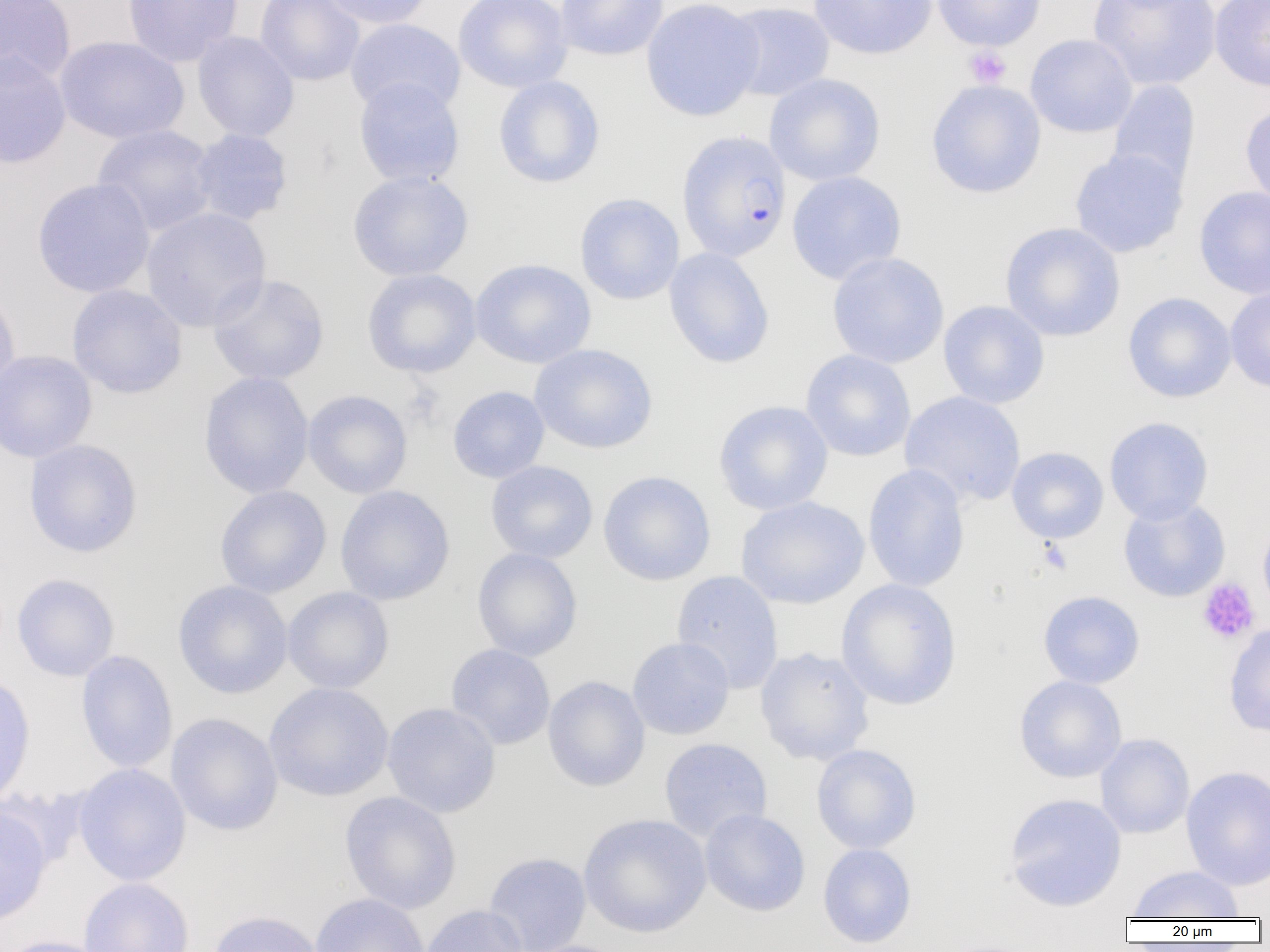

Summary:
  - Coordinate format: approximate bounding boxes as named x1/y1/x2/y2 corners in pixels
  - Uninfected red blood cell locations (subset): (x1=0, y1=0, x2=76, y2=87), (x1=122, y1=0, x2=243, y2=67), (x1=256, y1=0, x2=365, y2=86), (x1=319, y1=0, x2=431, y2=28), (x1=453, y1=0, x2=572, y2=93), (x1=555, y1=0, x2=669, y2=61), (x1=641, y1=0, x2=765, y2=121), (x1=808, y1=0, x2=938, y2=60), (x1=932, y1=0, x2=1046, y2=51), (x1=1210, y1=0, x2=1270, y2=92), (x1=1088, y1=1, x2=1221, y2=90), (x1=722, y1=2, x2=835, y2=101), (x1=345, y1=18, x2=465, y2=117), (x1=192, y1=31, x2=299, y2=142), (x1=1025, y1=34, x2=1138, y2=138), (x1=54, y1=36, x2=189, y2=144), (x1=0, y1=51, x2=72, y2=169), (x1=764, y1=73, x2=885, y2=186), (x1=493, y1=75, x2=606, y2=188), (x1=353, y1=77, x2=465, y2=188), (x1=926, y1=79, x2=1046, y2=199), (x1=1107, y1=79, x2=1201, y2=192), (x1=1240, y1=100, x2=1270, y2=211), (x1=92, y1=124, x2=218, y2=237), (x1=187, y1=128, x2=294, y2=226), (x1=1069, y1=148, x2=1188, y2=258), (x1=347, y1=171, x2=473, y2=281), (x1=786, y1=171, x2=907, y2=284), (x1=32, y1=178, x2=155, y2=298), (x1=1194, y1=185, x2=1270, y2=300), (x1=574, y1=193, x2=685, y2=305), (x1=141, y1=207, x2=272, y2=332), (x1=1000, y1=222, x2=1125, y2=342), (x1=663, y1=247, x2=775, y2=368), (x1=827, y1=252, x2=949, y2=368), (x1=470, y1=258, x2=596, y2=368), (x1=361, y1=268, x2=482, y2=378), (x1=207, y1=273, x2=329, y2=385), (x1=66, y1=284, x2=188, y2=399), (x1=1225, y1=284, x2=1270, y2=394), (x1=0, y1=285, x2=21, y2=404), (x1=1123, y1=292, x2=1237, y2=403), (x1=938, y1=300, x2=1050, y2=409), (x1=529, y1=343, x2=658, y2=454), (x1=0, y1=349, x2=98, y2=463), (x1=801, y1=349, x2=916, y2=462), (x1=198, y1=371, x2=314, y2=499), (x1=447, y1=385, x2=550, y2=483), (x1=302, y1=389, x2=413, y2=499), (x1=899, y1=391, x2=1026, y2=508), (x1=713, y1=400, x2=833, y2=515), (x1=1104, y1=416, x2=1214, y2=524), (x1=23, y1=439, x2=143, y2=558), (x1=1006, y1=446, x2=1109, y2=544), (x1=485, y1=460, x2=598, y2=563), (x1=862, y1=464, x2=971, y2=592), (x1=481, y1=466, x2=714, y2=568), (x1=597, y1=470, x2=716, y2=586), (x1=214, y1=485, x2=332, y2=599), (x1=335, y1=485, x2=455, y2=605), (x1=735, y1=496, x2=870, y2=609), (x1=1257, y1=517, x2=1270, y2=623), (x1=472, y1=547, x2=583, y2=662), (x1=670, y1=570, x2=784, y2=693), (x1=12, y1=573, x2=120, y2=682), (x1=836, y1=578, x2=962, y2=710), (x1=172, y1=580, x2=293, y2=699), (x1=282, y1=587, x2=394, y2=694), (x1=1038, y1=590, x2=1145, y2=689), (x1=1224, y1=622, x2=1270, y2=737), (x1=627, y1=637, x2=735, y2=740), (x1=446, y1=644, x2=556, y2=750), (x1=754, y1=647, x2=875, y2=766), (x1=75, y1=650, x2=178, y2=773), (x1=0, y1=671, x2=35, y2=811), (x1=1014, y1=675, x2=1127, y2=783), (x1=542, y1=676, x2=650, y2=792), (x1=263, y1=682, x2=394, y2=802), (x1=382, y1=702, x2=501, y2=818), (x1=165, y1=713, x2=283, y2=836), (x1=1095, y1=733, x2=1194, y2=839), (x1=658, y1=737, x2=772, y2=842), (x1=811, y1=743, x2=922, y2=854), (x1=73, y1=763, x2=192, y2=886), (x1=1180, y1=765, x2=1270, y2=890), (x1=339, y1=791, x2=462, y2=915), (x1=1004, y1=793, x2=1127, y2=911), (x1=0, y1=804, x2=53, y2=928), (x1=700, y1=808, x2=811, y2=917), (x1=578, y1=813, x2=712, y2=938), (x1=817, y1=843, x2=917, y2=948), (x1=483, y1=852, x2=592, y2=952), (x1=1127, y1=866, x2=1245, y2=921), (x1=79, y1=878, x2=194, y2=952), (x1=310, y1=893, x2=430, y2=952), (x1=420, y1=905, x2=529, y2=952), (x1=207, y1=910, x2=324, y2=952), (x1=0, y1=935, x2=115, y2=952)
  - Plasmodium falciparum-infected red blood cell locations: (x1=675, y1=129, x2=791, y2=262)
  - Platelet locations (subset): (x1=963, y1=45, x2=1012, y2=89), (x1=1038, y1=539, x2=1072, y2=574), (x1=1197, y1=578, x2=1260, y2=645)
  - Slide-level diagnosis: Plasmodium falciparum
  - Preparation: thin blood film
  - Modality: light microscopy
  - Magnification: 1000x
  - Image size: 1270×952 pixels
  - Field of view: single